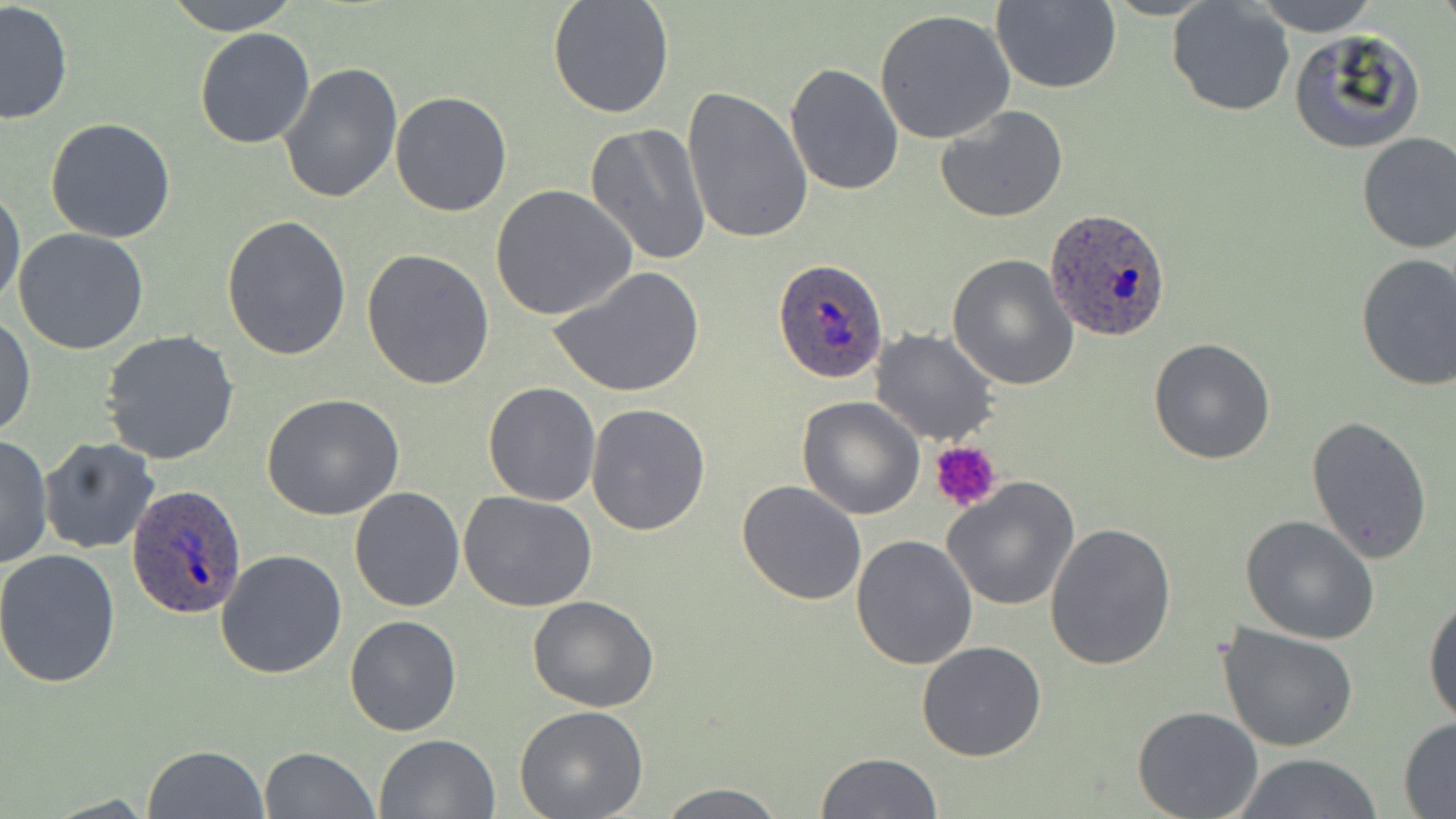

slide_level_diagnosis: Plasmodium ovale
image_size: 1456×819 pixels
preparation: thin blood film
plasmodium_ovale_infected_red_blood_cell_locations: 'approximate bounding boxes as (x1,y1)-(x2,y2) corner pairs in pixels: (1045,209)-(1171,343), (772,258)-(889,384), (125,482)-(249,619)'
field_of_view: single
stain: May-Grünwald-Giemsa
modality: light microscopy
platelet_locations: 'approximate bounding boxes as (x1,y1)-(x2,y2) corner pairs in pixels: (932,442)-(1002,513)'
magnification: 1000x
uninfected_red_blood_cell_locations: 'approximate bounding boxes as (x1,y1)-(x2,y2) corner pairs in pixels: (164,0)-(302,36), (547,0)-(675,118), (990,0)-(1121,94), (1166,0)-(1294,117), (1253,0)-(1381,37), (0,2)-(74,126), (875,9)-(1017,145), (193,27)-(316,149), (1288,28)-(1426,155), (277,61)-(402,204), (784,63)-(904,196), (682,84)-(813,244), (388,91)-(513,215), (935,104)-(1069,222), (45,118)-(178,244), (585,123)-(713,265), (1356,132)-(1456,254), (492,184)-(637,323), (0,187)-(24,311), (220,215)-(351,361), (13,228)-(149,354), (362,247)-(496,390), (947,253)-(1079,390), (1354,253)-(1456,390), (549,265)-(706,399), (0,314)-(36,439), (870,327)-(999,445), (100,329)-(240,465), (1148,338)-(1276,464), (481,380)-(601,505), (260,393)-(407,521), (797,395)-(925,519), (587,404)-(711,535), (1305,415)-(1434,562), (0,434)-(52,572), (39,438)-(160,555), (942,475)-(1082,611), (736,480)-(868,605), (349,487)-(466,612), (458,490)-(598,611), (1241,515)-(1383,644), (1045,522)-(1177,672), (850,533)-(980,670), (0,550)-(123,689), (216,550)-(348,679), (1423,590)-(1456,730), (528,596)-(658,712), (345,614)-(462,737), (1219,623)-(1358,754), (916,639)-(1046,761), (514,706)-(648,818), (1131,706)-(1264,819), (1398,717)-(1456,815), (373,732)-(501,819), (143,744)-(267,818), (259,746)-(378,818), (813,751)-(946,818), (1228,753)-(1385,818), (653,783)-(788,818)'